Classify this cell by malaria status.
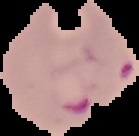

Parasitized.

Summary:
  - Preparation: thin blood smear
  - Image type: segmented cell region on a black background
  - Image size: 139×136 pixels